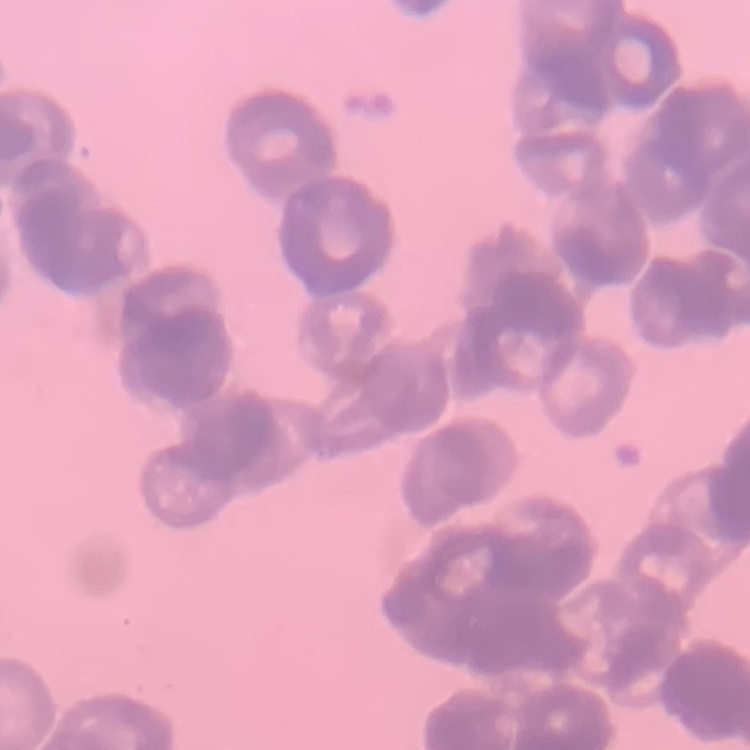
The red blood cells exhibit rouleaux formation. Field's or Giemsa stain. Square crop of a larger photomicrograph. Thin blood film.